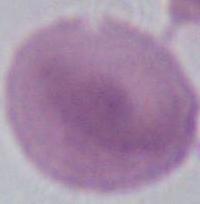

Summary:
  - Identification: erythrocyte
  - Modality: micrograph
  - Magnification: 1000x